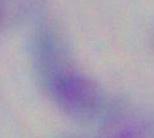
modality = photomicrograph
identification = Toxoplasma gondii
magnification = 1000x